Comment on the morphology of the erythrocytes.
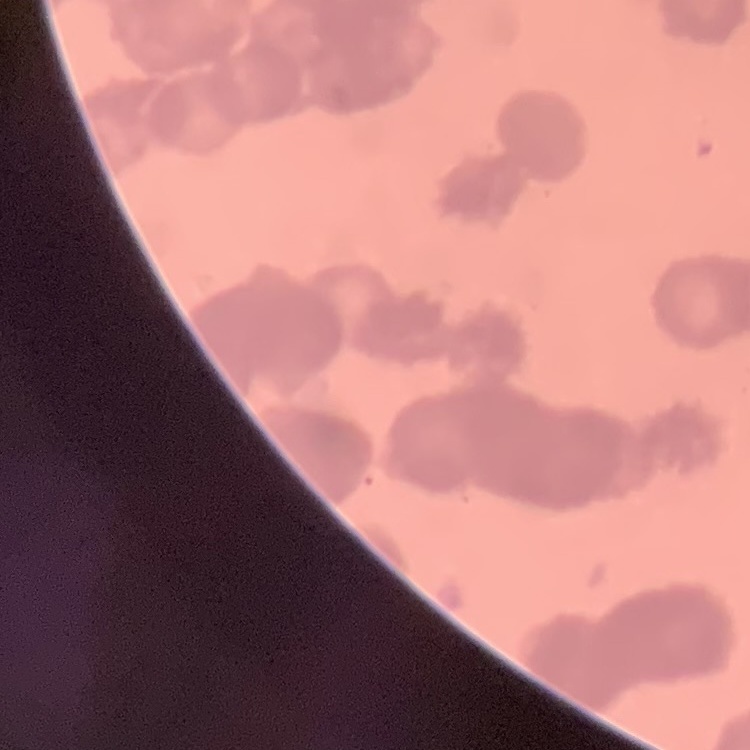

Rouleaux formation.

Field's or Giemsa stain. One tile cut from a larger photomicrograph. Thin blood film.